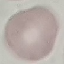
{
  "malaria_status": "uninfected",
  "capture": "smartphone through the microscope eyepiece",
  "image_type": "automatically extracted cell patch, resized to 64 × 64 pixels",
  "stain": "Giemsa",
  "preparation": "thin smear"
}